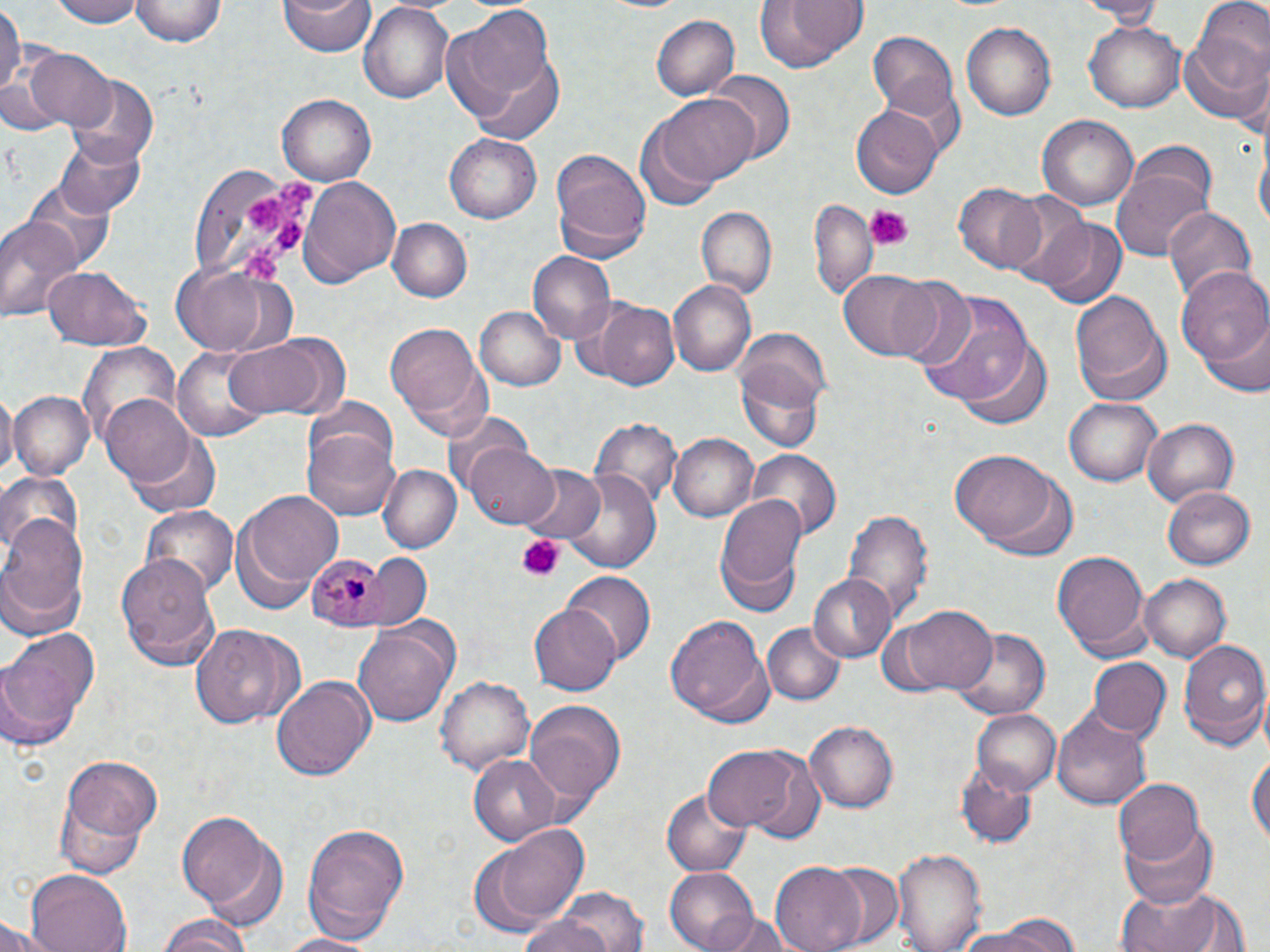

Approximate bounding boxes as named x1/y1/x2/y2 corners in pixels. Plasmodium malariae-infected red blood cell locations: (x1=304, y1=549, x2=389, y2=629). Uninfected red blood cell locations: (x1=0, y1=0, x2=21, y2=99), (x1=50, y1=0, x2=142, y2=28), (x1=132, y1=0, x2=224, y2=48), (x1=279, y1=0, x2=374, y2=57), (x1=754, y1=0, x2=868, y2=70), (x1=1072, y1=0, x2=1168, y2=23), (x1=359, y1=1, x2=453, y2=104), (x1=1197, y1=2, x2=1270, y2=81), (x1=444, y1=9, x2=562, y2=136), (x1=651, y1=15, x2=739, y2=102), (x1=1181, y1=18, x2=1268, y2=127), (x1=1085, y1=20, x2=1184, y2=112), (x1=962, y1=21, x2=1057, y2=120), (x1=868, y1=33, x2=959, y2=119), (x1=25, y1=48, x2=116, y2=132), (x1=707, y1=73, x2=793, y2=165), (x1=69, y1=76, x2=157, y2=169), (x1=276, y1=94, x2=375, y2=187), (x1=655, y1=94, x2=759, y2=188), (x1=852, y1=103, x2=944, y2=199), (x1=1037, y1=115, x2=1138, y2=212), (x1=635, y1=121, x2=720, y2=213), (x1=55, y1=127, x2=147, y2=216), (x1=447, y1=135, x2=539, y2=225), (x1=1255, y1=140, x2=1269, y2=238), (x1=551, y1=148, x2=652, y2=260), (x1=1112, y1=164, x2=1211, y2=262), (x1=191, y1=167, x2=318, y2=290), (x1=299, y1=176, x2=401, y2=286), (x1=22, y1=177, x2=118, y2=274), (x1=956, y1=183, x2=1049, y2=274), (x1=811, y1=199, x2=878, y2=296), (x1=695, y1=206, x2=777, y2=297), (x1=1162, y1=206, x2=1258, y2=305), (x1=0, y1=214, x2=81, y2=324), (x1=1031, y1=214, x2=1124, y2=302), (x1=390, y1=218, x2=471, y2=301), (x1=528, y1=252, x2=615, y2=345), (x1=169, y1=260, x2=286, y2=359), (x1=40, y1=265, x2=150, y2=351), (x1=1179, y1=267, x2=1270, y2=387), (x1=838, y1=269, x2=940, y2=361), (x1=887, y1=276, x2=977, y2=369), (x1=668, y1=280, x2=757, y2=377), (x1=914, y1=292, x2=1038, y2=406), (x1=1070, y1=292, x2=1171, y2=404), (x1=596, y1=300, x2=677, y2=387), (x1=474, y1=304, x2=564, y2=392), (x1=385, y1=322, x2=488, y2=437), (x1=1197, y1=322, x2=1270, y2=395), (x1=735, y1=328, x2=832, y2=415), (x1=223, y1=336, x2=327, y2=419), (x1=957, y1=339, x2=1053, y2=429), (x1=77, y1=341, x2=183, y2=446), (x1=170, y1=346, x2=278, y2=442), (x1=736, y1=359, x2=826, y2=455), (x1=0, y1=390, x2=16, y2=481), (x1=11, y1=391, x2=92, y2=479), (x1=101, y1=395, x2=199, y2=488), (x1=1064, y1=396, x2=1162, y2=486), (x1=302, y1=398, x2=400, y2=483), (x1=441, y1=411, x2=531, y2=496), (x1=593, y1=418, x2=679, y2=508), (x1=1142, y1=419, x2=1239, y2=505), (x1=301, y1=427, x2=401, y2=520), (x1=670, y1=433, x2=760, y2=521), (x1=128, y1=435, x2=222, y2=517), (x1=465, y1=442, x2=560, y2=529), (x1=748, y1=449, x2=839, y2=539), (x1=953, y1=451, x2=1059, y2=548), (x1=377, y1=464, x2=461, y2=552), (x1=518, y1=465, x2=605, y2=547), (x1=561, y1=469, x2=663, y2=573), (x1=0, y1=473, x2=82, y2=559), (x1=1164, y1=486, x2=1255, y2=569), (x1=240, y1=488, x2=342, y2=593), (x1=715, y1=496, x2=806, y2=611), (x1=139, y1=506, x2=239, y2=596), (x1=845, y1=508, x2=931, y2=625), (x1=0, y1=513, x2=88, y2=625), (x1=1052, y1=547, x2=1150, y2=654), (x1=118, y1=552, x2=220, y2=670), (x1=371, y1=554, x2=434, y2=629), (x1=805, y1=571, x2=898, y2=662), (x1=562, y1=572, x2=656, y2=664), (x1=1139, y1=573, x2=1231, y2=662), (x1=898, y1=605, x2=998, y2=695), (x1=529, y1=606, x2=620, y2=695), (x1=664, y1=614, x2=774, y2=727), (x1=762, y1=622, x2=845, y2=705), (x1=194, y1=623, x2=295, y2=732), (x1=354, y1=623, x2=456, y2=728), (x1=952, y1=624, x2=1053, y2=719), (x1=0, y1=626, x2=101, y2=751), (x1=1177, y1=636, x2=1270, y2=751), (x1=1089, y1=658, x2=1169, y2=740), (x1=271, y1=676, x2=375, y2=781), (x1=435, y1=676, x2=534, y2=777), (x1=524, y1=701, x2=627, y2=807), (x1=1053, y1=707, x2=1154, y2=812), (x1=973, y1=709, x2=1061, y2=795), (x1=806, y1=721, x2=899, y2=813), (x1=703, y1=745, x2=806, y2=834), (x1=1247, y1=748, x2=1269, y2=855), (x1=469, y1=753, x2=561, y2=846), (x1=57, y1=755, x2=162, y2=869), (x1=956, y1=761, x2=1035, y2=847), (x1=1113, y1=779, x2=1205, y2=865), (x1=660, y1=789, x2=752, y2=876), (x1=177, y1=809, x2=280, y2=924), (x1=1122, y1=817, x2=1218, y2=909), (x1=469, y1=821, x2=591, y2=935), (x1=300, y1=823, x2=410, y2=943), (x1=893, y1=845, x2=982, y2=952), (x1=772, y1=862, x2=867, y2=952), (x1=823, y1=862, x2=902, y2=946), (x1=664, y1=866, x2=763, y2=952), (x1=24, y1=869, x2=132, y2=952), (x1=1116, y1=881, x2=1247, y2=952), (x1=545, y1=885, x2=653, y2=952), (x1=517, y1=909, x2=617, y2=952), (x1=959, y1=911, x2=1079, y2=952), (x1=156, y1=915, x2=252, y2=952), (x1=714, y1=915, x2=796, y2=952), (x1=0, y1=916, x2=56, y2=952), (x1=272, y1=930, x2=384, y2=951). Platelet locations: (x1=276, y1=175, x2=313, y2=214), (x1=245, y1=195, x2=285, y2=233), (x1=864, y1=205, x2=913, y2=249), (x1=271, y1=219, x2=305, y2=250), (x1=241, y1=244, x2=285, y2=281), (x1=517, y1=535, x2=566, y2=581). Slide-level diagnosis: Plasmodium malariae. May-Grünwald-Giemsa-stained preparation. 1000x magnification. Thin blood smear. Optical microscopy. Image is 1270×952 pixels. Single field of view.